Assess this cell for malaria.
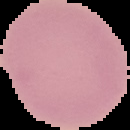

Uninfected.

preparation = thin blood smear
image type = segmented cell region on a black background
image size = 130×130 pixels